State the blood parasite species.
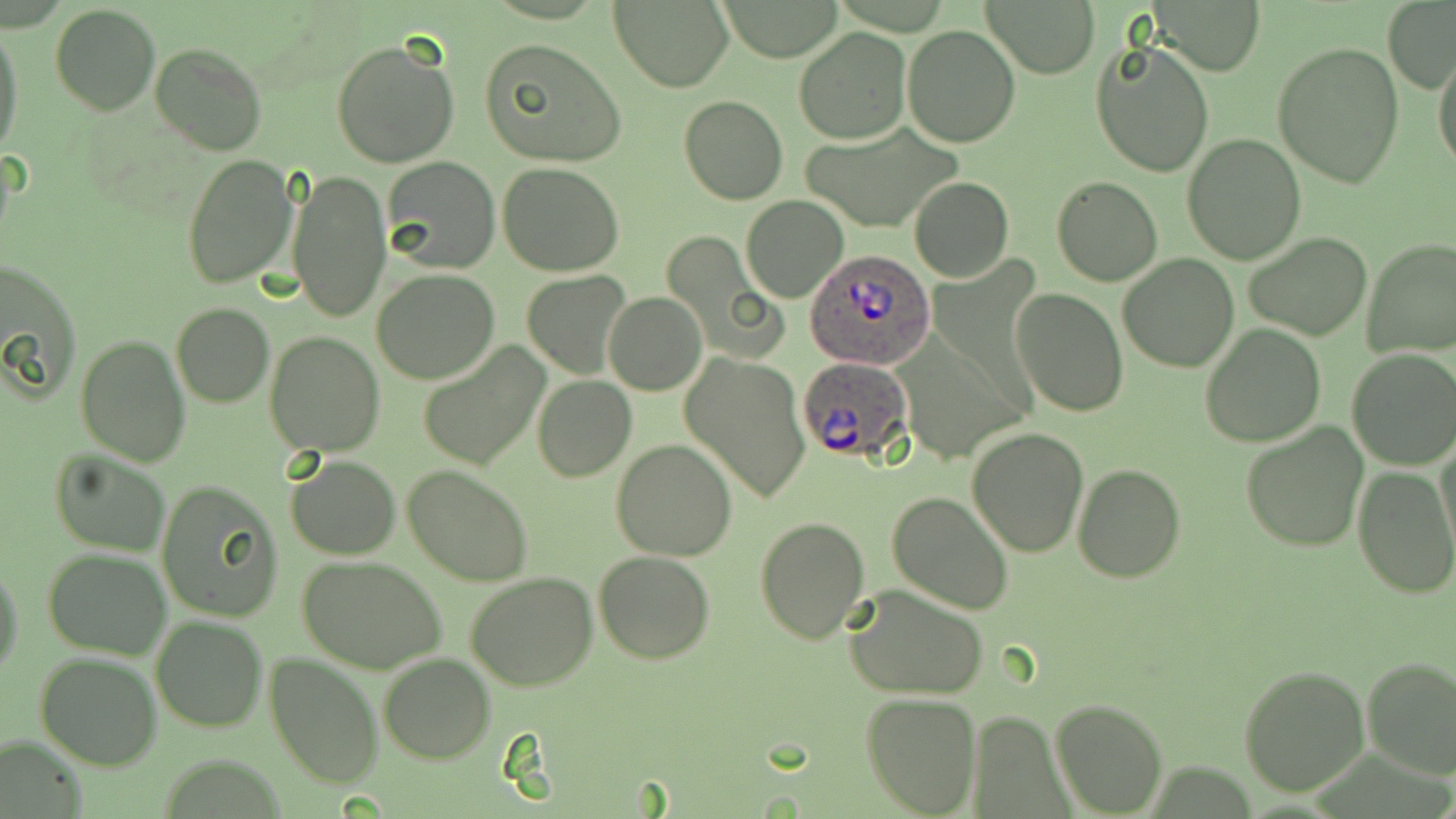

Plasmodium ovale.

Summary:
  - Coordinate format: approximate bounding boxes as (x1,y1)-(x2,y2) corner pairs in pixels
  - Uninfected red blood cell locations: (718,0)-(846,60), (610,1)-(733,90), (981,1)-(1099,78), (1156,1)-(1264,75), (1382,2)-(1454,92), (50,5)-(160,115), (0,23)-(24,164), (902,24)-(1020,147), (795,29)-(910,145), (1090,35)-(1216,177), (480,37)-(628,167), (331,39)-(460,170), (1272,40)-(1404,188), (149,43)-(267,157), (1432,45)-(1456,175), (679,94)-(788,205), (800,123)-(961,230), (1182,133)-(1306,263), (181,154)-(300,290), (383,157)-(500,273), (500,162)-(622,276), (288,169)-(391,323), (1052,176)-(1163,286), (909,177)-(1014,283), (742,197)-(849,303), (1244,231)-(1372,340), (1361,239)-(1456,358), (1118,253)-(1238,372), (1,258)-(81,401), (372,270)-(498,384), (521,272)-(627,377), (1010,287)-(1128,416), (605,291)-(706,396), (171,302)-(274,406), (1200,324)-(1326,447), (264,332)-(385,458), (74,334)-(192,467), (417,342)-(550,473), (1347,348)-(1456,470), (683,352)-(810,504), (532,376)-(636,482), (1239,421)-(1370,554), (967,428)-(1089,557), (1435,436)-(1456,558), (611,439)-(737,562), (49,449)-(171,558), (286,454)-(399,560), (1073,462)-(1186,582), (402,465)-(534,586), (1353,465)-(1456,598), (156,480)-(283,622), (886,490)-(1015,616), (754,515)-(871,643), (42,549)-(172,659), (592,550)-(716,663), (297,554)-(449,675), (0,561)-(24,682), (464,571)-(598,692), (845,583)-(991,699), (151,616)-(267,731), (35,651)-(162,769), (265,653)-(384,788), (379,653)-(495,764), (1361,656)-(1456,778), (1238,666)-(1369,795), (860,691)-(981,817), (1052,698)-(1167,816), (1,733)-(85,819)
  - Plasmodium ovale-infected red blood cell locations: (806,249)-(937,369), (797,356)-(913,462)
  - Magnification: 1000x
  - Preparation: thin blood smear
  - Modality: optical microscopy
  - Stain: May-Grünwald-Giemsa
  - Image size: 1456×819 pixels
  - Field of view: single